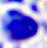
modality = photomicrograph
identification = white blood cell
magnification = 400x